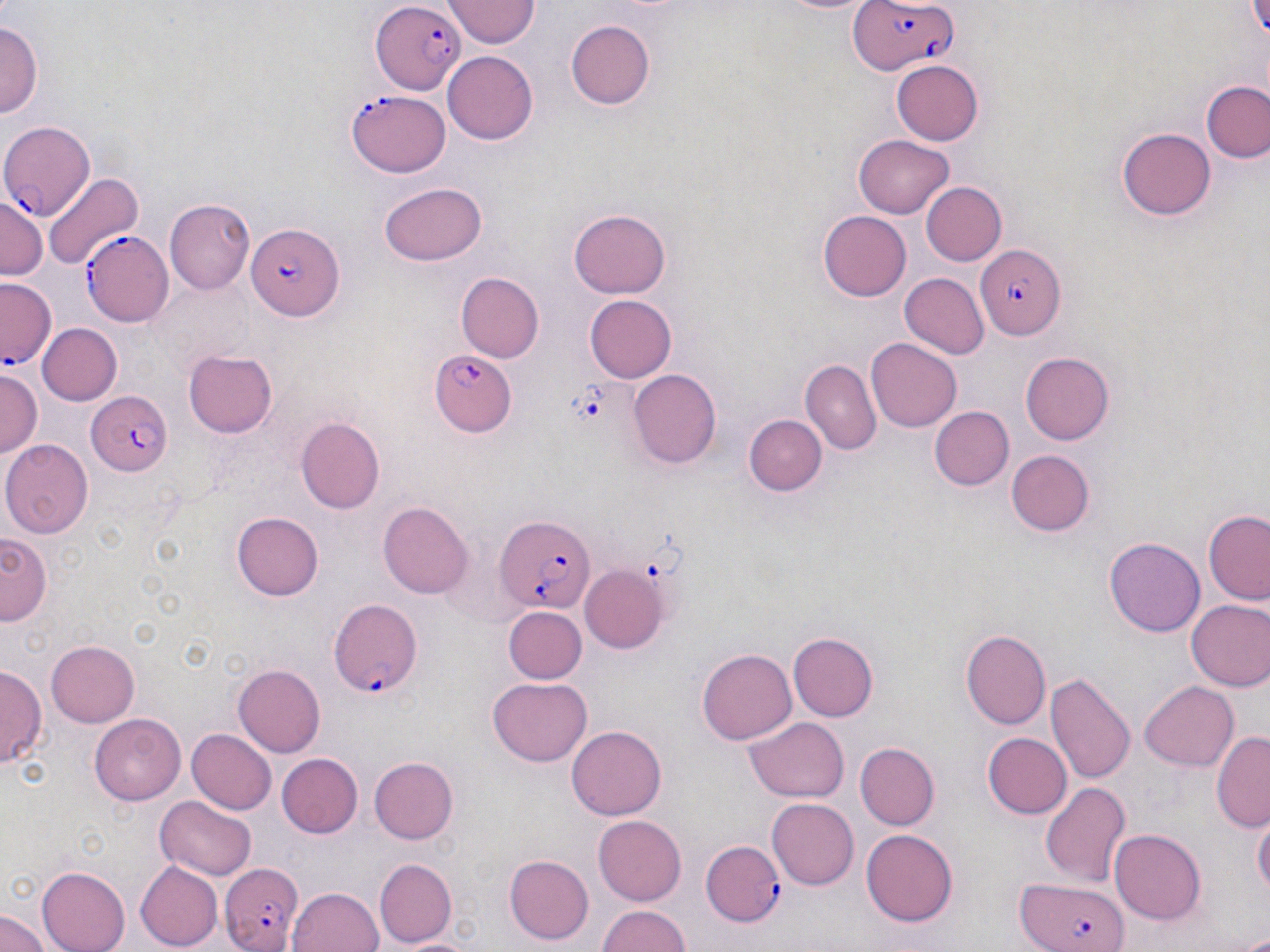
{
  "slide_level_diagnosis": "Plasmodium falciparum",
  "image_size": "1270×952 pixels",
  "field_of_view": "one of a larger specimen",
  "stain": "May-Grünwald-Giemsa",
  "modality": "optical microscopy",
  "magnification": "1000x",
  "uninfected_red_blood_cell_locations": "approximate bounding boxes as (x1, y1, x2, y2) in pixels: (446, 2, 541, 47), (565, 19, 655, 109), (1, 21, 41, 117), (443, 52, 538, 144), (893, 60, 986, 144), (1204, 82, 1270, 165), (1119, 126, 1215, 217), (853, 136, 956, 218), (41, 170, 144, 275), (920, 181, 1005, 266), (380, 182, 488, 265), (0, 194, 47, 277), (168, 199, 255, 294), (570, 209, 673, 299), (817, 210, 911, 301), (455, 273, 544, 363), (900, 273, 988, 360), (155, 283, 246, 370), (583, 294, 677, 382), (39, 323, 121, 403), (867, 338, 962, 431), (1017, 349, 1118, 444), (183, 350, 277, 438), (800, 352, 956, 444), (801, 361, 880, 453), (1, 367, 43, 458), (629, 370, 721, 469), (931, 407, 1015, 491), (742, 414, 828, 497), (296, 418, 385, 514), (3, 440, 92, 538), (1003, 447, 1098, 537), (379, 502, 472, 598), (1202, 503, 1270, 608), (232, 511, 323, 601), (0, 532, 49, 623), (1105, 537, 1202, 636), (581, 567, 668, 652), (1186, 598, 1270, 693), (503, 607, 587, 684), (962, 629, 1051, 731), (787, 631, 878, 723), (47, 641, 139, 726), (697, 649, 798, 745), (232, 665, 325, 759), (0, 666, 44, 766), (1046, 671, 1135, 787), (487, 678, 593, 766), (1140, 681, 1239, 771), (90, 714, 184, 805), (744, 717, 849, 804), (567, 725, 665, 820), (186, 728, 276, 815), (1211, 730, 1270, 832), (981, 733, 1071, 818), (856, 743, 939, 829), (278, 753, 362, 838), (369, 755, 458, 844), (1040, 780, 1131, 888), (153, 797, 257, 880), (768, 798, 858, 889), (1253, 812, 1269, 901), (594, 814, 687, 904), (1111, 828, 1207, 924), (861, 830, 958, 924), (503, 854, 594, 944), (375, 858, 458, 945), (136, 862, 222, 950), (36, 865, 131, 952), (289, 886, 384, 952), (595, 905, 692, 951), (0, 910, 48, 952)",
  "platelet_locations": "approximate bounding boxes as (x1, y1, x2, y2) in pixels: (570, 386, 608, 429)",
  "plasmodium_falciparum_infected_red_blood_cell_locations": "approximate bounding boxes as (x1, y1, x2, y2) in pixels: (847, 0, 962, 74), (370, 3, 464, 95), (347, 88, 450, 175), (0, 119, 95, 222), (245, 220, 342, 318), (83, 231, 172, 327), (975, 248, 1064, 340), (1, 276, 59, 371), (427, 351, 516, 437), (87, 390, 171, 476), (493, 513, 596, 614), (329, 593, 425, 696), (700, 842, 784, 928), (218, 861, 304, 952), (1018, 878, 1128, 952)",
  "preparation": "thin blood smear"
}